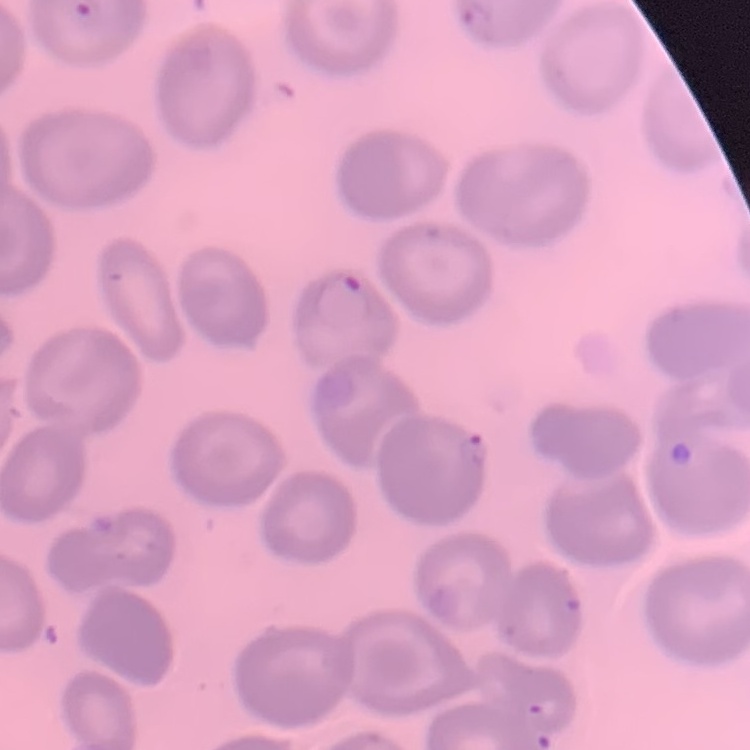

The erythrocytes exhibit no rouleaux formation. Thin blood film. Square crop of a larger photomicrograph. Stained with either Field's or Giemsa.